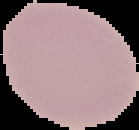

Summary:
  - Image type: segmented cell region on a black background
  - Preparation: thin blood film
  - Image size: 139×130 pixels
  - Malaria status: uninfected